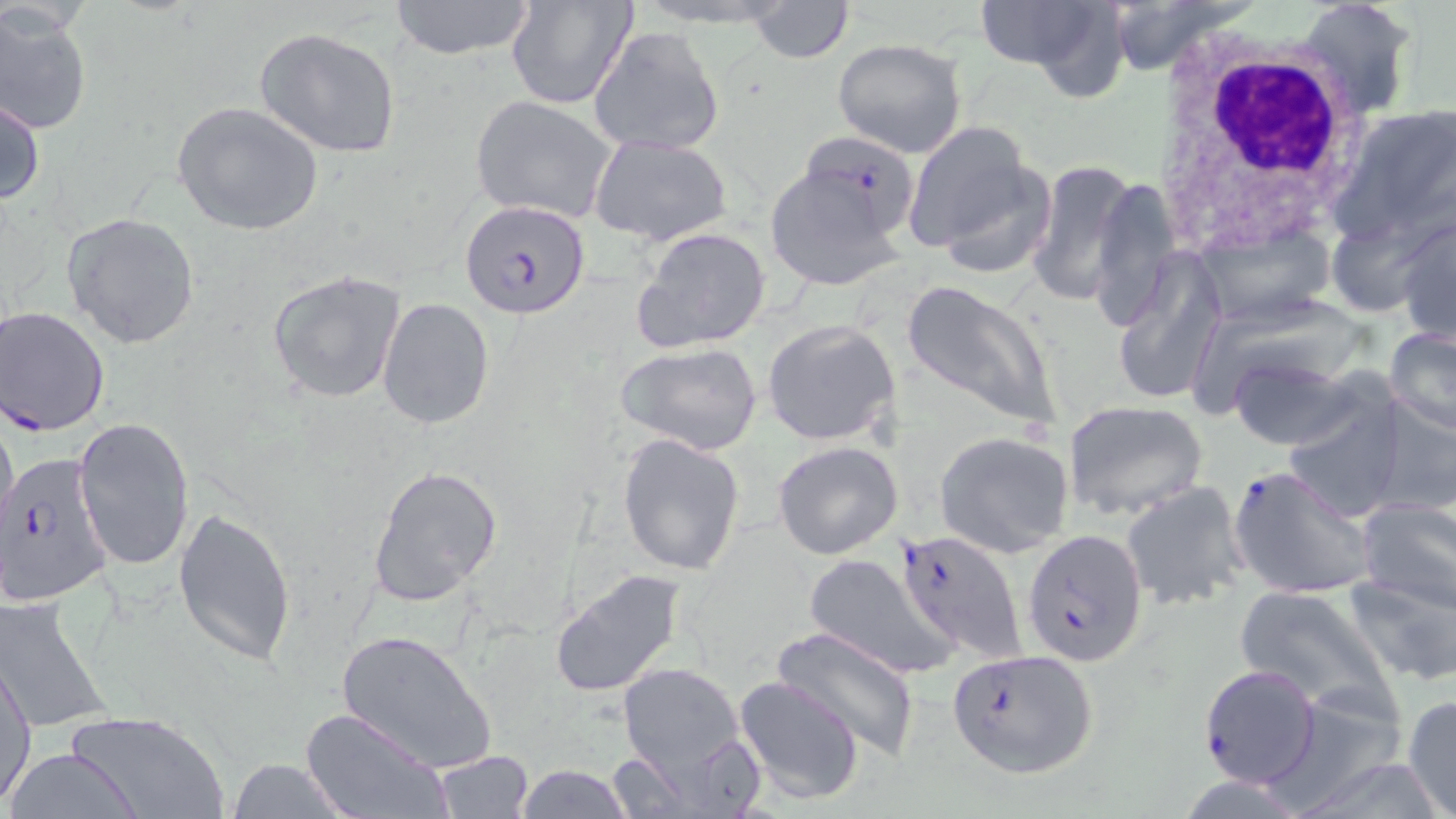 Approximate bounding boxes as [x1, y1, x2, y2] in pixels. Uninfected red blood cell locations: [386, 0, 540, 61], [505, 0, 638, 109], [746, 0, 854, 63], [972, 0, 1124, 87], [1106, 0, 1244, 76], [1296, 0, 1419, 119], [0, 5, 92, 136], [589, 26, 725, 157], [254, 27, 402, 158], [831, 37, 969, 158], [0, 95, 45, 209], [471, 95, 619, 224], [172, 101, 323, 235], [1332, 103, 1456, 245], [901, 119, 1047, 266], [589, 135, 733, 246], [765, 160, 907, 290], [1026, 160, 1140, 309], [1087, 175, 1183, 331], [1328, 199, 1450, 321], [1394, 210, 1455, 346], [62, 212, 200, 349], [1192, 223, 1334, 331], [632, 227, 771, 354], [1110, 247, 1228, 406], [266, 269, 407, 404], [900, 277, 1063, 431], [377, 297, 493, 431], [762, 320, 899, 447], [1385, 326, 1456, 437], [614, 342, 765, 458], [1223, 354, 1364, 452], [1280, 388, 1408, 522], [1369, 393, 1456, 520], [1061, 399, 1209, 522], [0, 407, 18, 543], [74, 417, 194, 571], [934, 431, 1075, 557], [617, 435, 746, 575], [773, 441, 904, 559], [367, 463, 503, 607], [1121, 482, 1249, 612], [1356, 498, 1455, 615], [174, 506, 296, 666], [804, 553, 959, 678], [550, 568, 687, 699], [1342, 571, 1456, 686], [1234, 585, 1397, 716], [0, 596, 112, 734], [770, 624, 924, 760], [337, 628, 496, 774], [1, 656, 36, 805], [617, 660, 750, 778], [735, 675, 865, 805], [1401, 694, 1456, 819], [1261, 695, 1414, 812], [299, 707, 449, 819], [65, 711, 229, 819], [4, 747, 146, 818], [603, 747, 705, 818], [1289, 749, 1439, 819], [432, 752, 534, 818], [227, 759, 351, 818], [512, 763, 634, 819]. Plasmodium falciparum-infected red blood cell locations: [802, 131, 922, 248], [460, 200, 592, 319], [1, 306, 111, 437], [0, 450, 117, 609], [1229, 464, 1379, 602], [894, 527, 1026, 662], [1020, 528, 1149, 666], [948, 644, 1101, 780], [1198, 663, 1322, 789]. White blood cell locations: [1153, 35, 1373, 251]. Slide-level diagnosis: Plasmodium falciparum. Single field of view. May-Grünwald-Giemsa-stained preparation. Image is 1456×819 pixels. 1000x magnification. Optical microscopy. Thin blood smear.